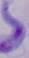
magnification = 1000x
identification = trypanosome
modality = micrograph